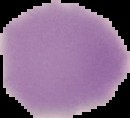
Summary:
  - Image size: 130×118 pixels
  - Preparation: thin blood smear
  - Image type: segmented cell region with the area outside set to black
  - Malaria status: uninfected